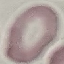
Malaria status: uninfected. Photographed with a smartphone camera at the microscope eyepiece. Cell patch, automatically extracted from a larger field of view and resized to 64 × 64 pixels. Giemsa-stained preparation. Thin blood smear.